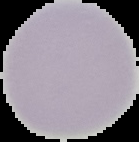
image type = segmented cell region on a black background
preparation = thin blood film
image size = 139×142 pixels
result = no Plasmodium parasites detected